Describe the morphology of the red blood cells.
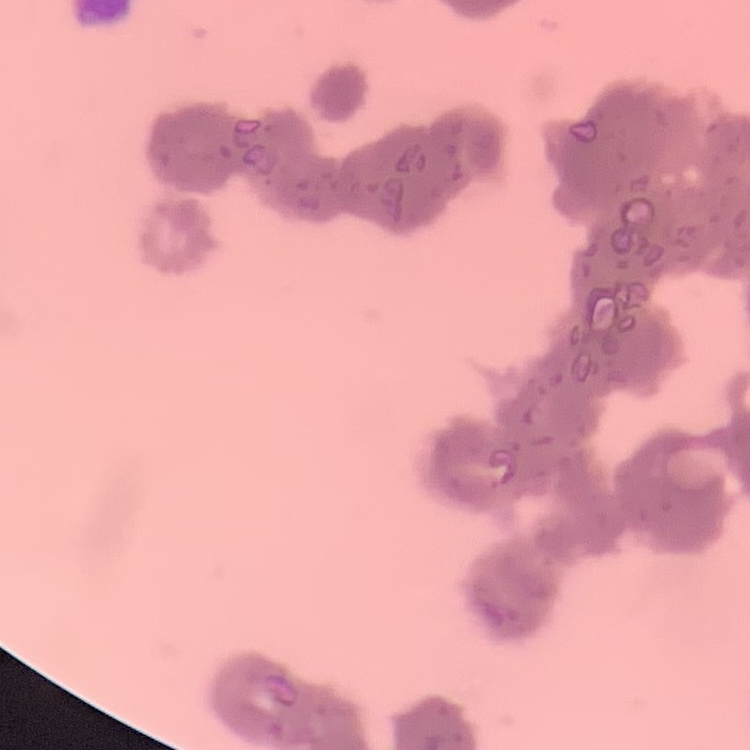
They show rouleaux formation.

preparation: thin blood film
image_type: square crop of a larger photomicrograph
stain: Field's or Giemsa